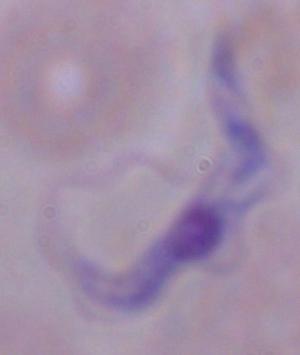

Summary:
  - Identification: trypanosome
  - Modality: photomicrograph
  - Magnification: 1000x